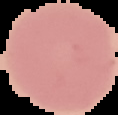

From a thin blood film. Cell region segmented out of the field of view; the surrounding area is masked to black. Result: no Plasmodium parasites seen. Image is 118×115 pixels.